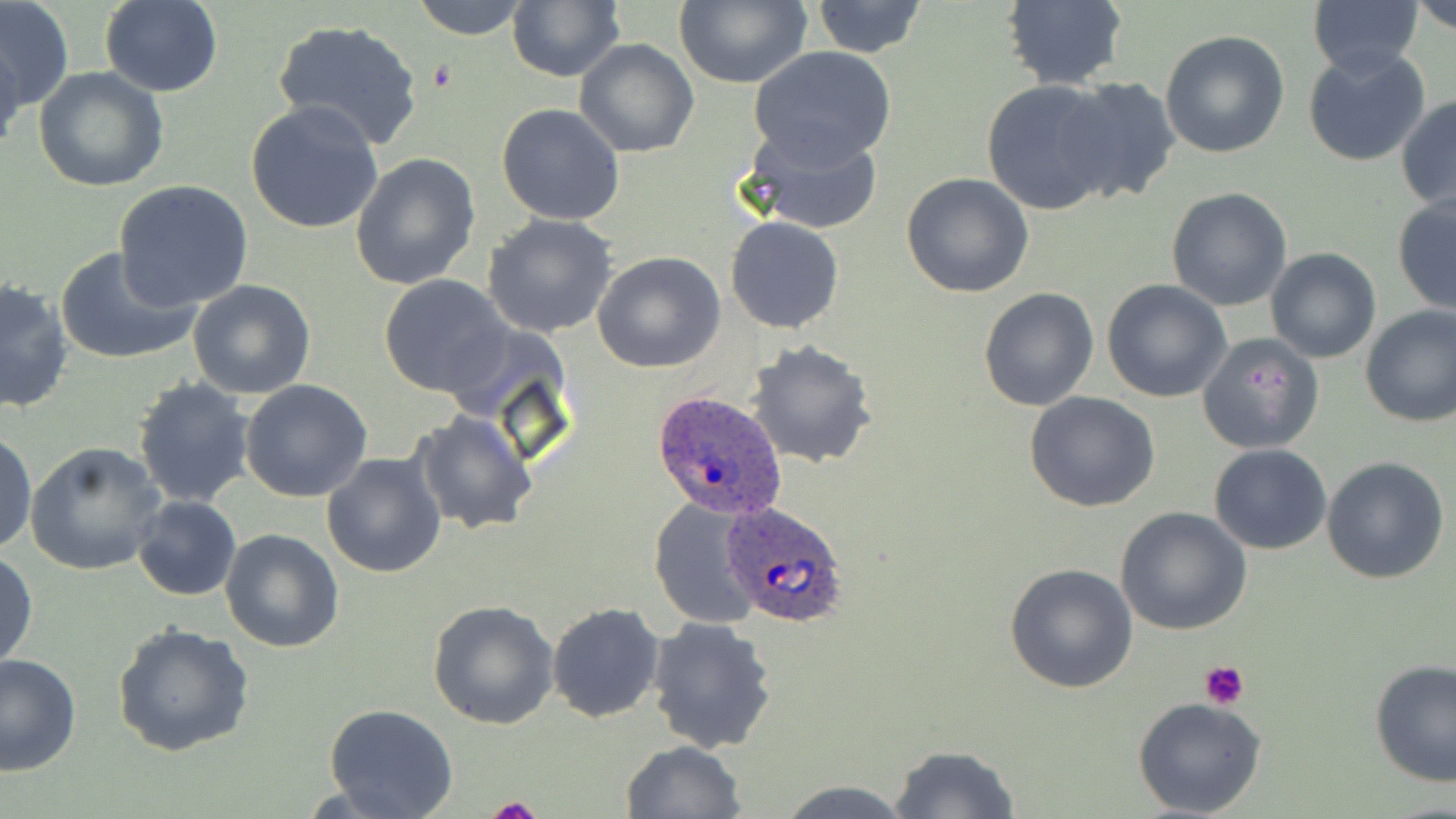
Approximate bounding boxes as (x1,y1)-(x2,y2) corner pairs in pixels. Plasmodium ovale-infected red blood cell locations: (650,392)-(788,520), (723,502)-(850,628). Platelet locations: (1199,661)-(1249,709), (486,794)-(544,819). Uninfected red blood cell locations: (1,0)-(74,113), (408,0)-(535,41), (507,0)-(626,82), (1308,0)-(1424,75), (1410,0)-(1456,33), (99,1)-(223,97), (809,1)-(927,57), (997,1)-(1129,90), (673,2)-(812,88), (272,18)-(424,150), (1160,30)-(1291,159), (0,36)-(24,155), (575,37)-(699,158), (749,46)-(898,167), (1302,46)-(1432,167), (34,67)-(168,192), (1056,77)-(1183,203), (980,79)-(1123,216), (1397,94)-(1456,213), (245,100)-(385,235), (495,102)-(625,226), (740,122)-(885,237), (349,152)-(480,289), (903,171)-(1034,297), (113,180)-(255,310), (1166,187)-(1294,311), (1392,196)-(1456,315), (483,214)-(621,337), (724,215)-(847,334), (55,246)-(199,365), (1264,247)-(1382,364), (593,252)-(726,373), (377,274)-(513,397), (1101,279)-(1233,403), (0,280)-(74,413), (187,280)-(317,401), (978,286)-(1100,411), (1359,303)-(1456,427), (1196,332)-(1325,455), (747,342)-(878,468), (131,376)-(256,507), (240,379)-(372,502), (1025,391)-(1162,513), (409,410)-(540,535), (1,430)-(37,555), (25,442)-(166,576), (1208,444)-(1332,554), (321,450)-(447,578), (1322,456)-(1450,583), (132,495)-(242,602), (648,497)-(765,627), (1116,507)-(1252,635), (219,528)-(344,653), (1,550)-(37,671), (1004,562)-(1138,693), (427,599)-(559,729), (546,601)-(666,722), (647,617)-(779,753), (112,623)-(255,759), (1,654)-(80,775), (1369,660)-(1456,788), (1132,698)-(1266,818), (323,703)-(458,819), (621,740)-(746,818), (889,744)-(1021,818), (777,781)-(914,817). Slide-level diagnosis: Plasmodium ovale. May-Grünwald-Giemsa-stained preparation. 1000x magnification. Light microscopy. Thin blood smear. One field of a larger specimen. Image is 1456×819 pixels.